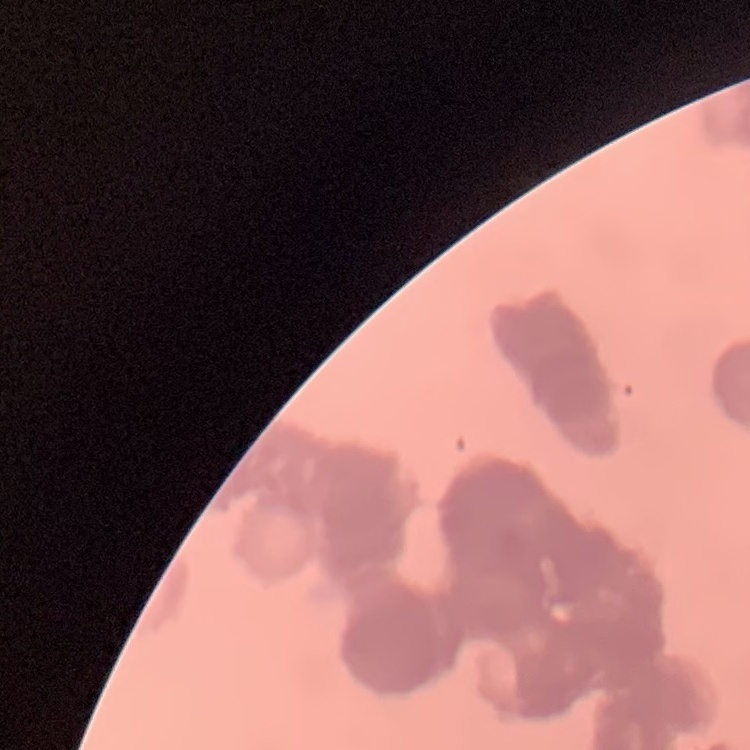

The erythrocytes exhibit rouleaux formation. Field's or Giemsa stain. Thin peripheral smear. One tile cut from a larger photomicrograph.